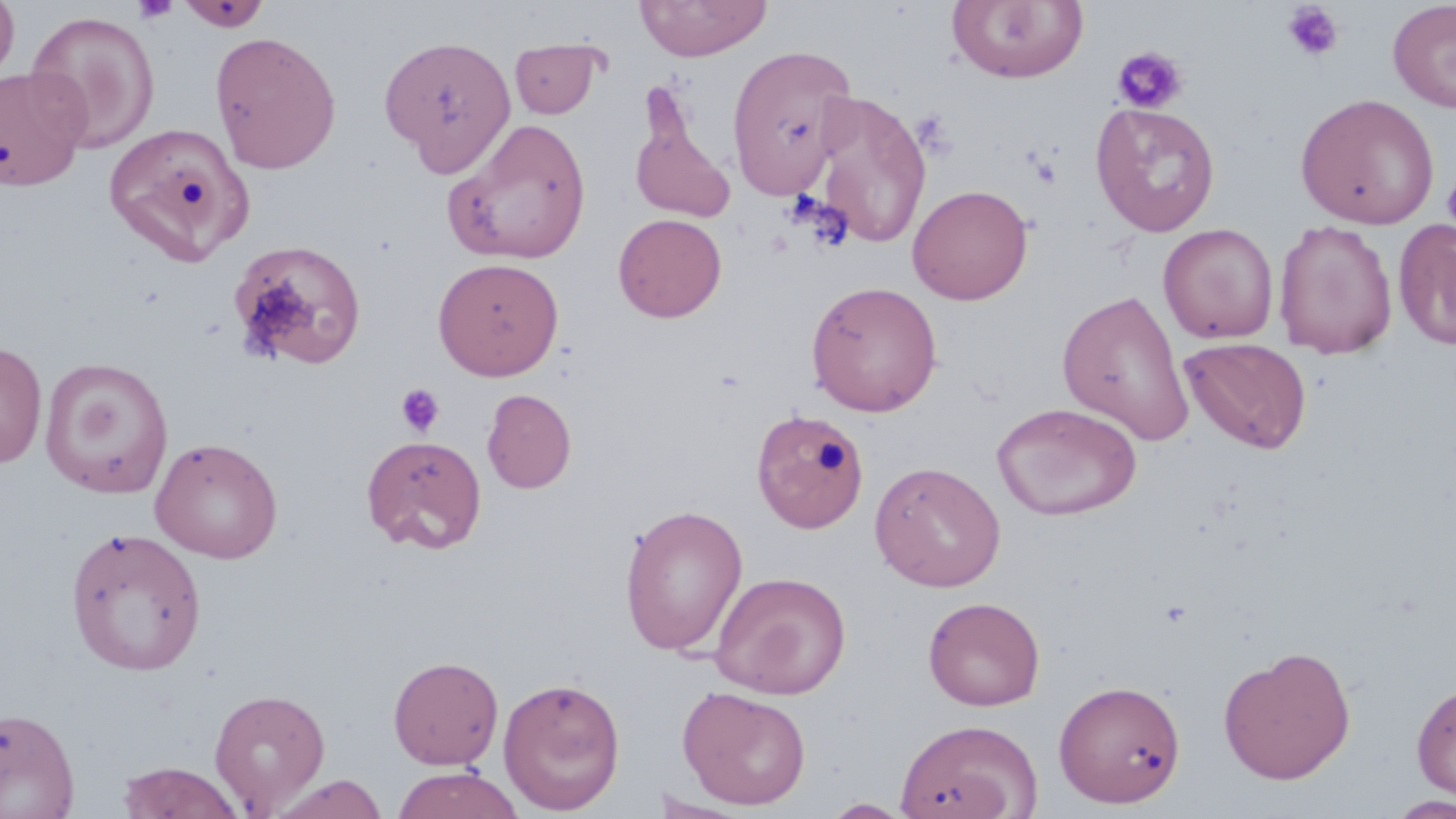

Approximate bounding boxes as [x1, y1, x2, y2] in pixels. Uninfected red blood cell locations: [0, 0, 19, 87], [635, 0, 772, 61], [1388, 0, 1456, 113], [177, 1, 271, 31], [946, 1, 1089, 83], [25, 11, 160, 153], [209, 31, 341, 174], [379, 35, 516, 174], [509, 37, 605, 119], [725, 45, 858, 199], [0, 66, 90, 191], [810, 88, 932, 251], [1295, 93, 1440, 229], [630, 95, 737, 224], [1089, 102, 1221, 237], [443, 118, 593, 266], [102, 121, 254, 266], [907, 184, 1033, 305], [613, 213, 727, 322], [1395, 218, 1456, 351], [1273, 219, 1398, 359], [1158, 223, 1278, 344], [228, 240, 367, 370], [433, 257, 564, 380], [805, 280, 943, 416], [1057, 288, 1195, 446], [1180, 337, 1313, 454], [0, 340, 47, 469], [40, 357, 173, 498], [482, 389, 576, 494], [992, 402, 1143, 522], [750, 408, 867, 535], [361, 434, 487, 554], [149, 437, 283, 563], [870, 461, 1006, 592], [619, 503, 749, 656], [65, 525, 206, 676], [710, 570, 851, 699], [923, 596, 1046, 711], [1218, 645, 1357, 785], [388, 655, 504, 769], [498, 676, 626, 814], [1053, 679, 1186, 808], [1411, 680, 1456, 803], [677, 685, 812, 810], [208, 687, 331, 814], [0, 706, 80, 819], [895, 718, 1043, 819], [117, 761, 245, 819], [391, 766, 525, 818], [270, 774, 388, 819], [650, 792, 755, 817], [1387, 795, 1456, 818], [821, 799, 915, 818]. Platelet locations: [132, 0, 179, 24], [1282, 3, 1345, 61], [1112, 46, 1188, 115], [911, 109, 956, 158], [1028, 152, 1061, 189], [1442, 172, 1456, 234], [395, 383, 445, 437]. Slide-level diagnosis: no evidence of blood parasites. 1000x magnification. Thin blood smear. Optical microscopy. May-Grünwald-Giemsa-stained preparation. Image is 1456×819 pixels. One field of a larger specimen.